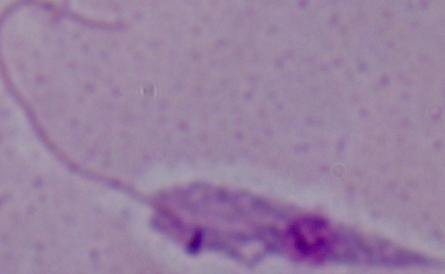
Summary:
  - Modality: micrograph
  - Magnification: 1000x
  - Identification: Leishmania